Report the malaria status of this cell.
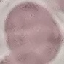

It is uninfected.

Photographed with a smartphone camera at the microscope eyepiece. Giemsa stain. Thin smear of blood. Automatically extracted cell patch, resized to 64 × 64 pixels.